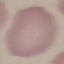
Summary:
  - Malaria status: uninfected
  - Stain: Giemsa
  - Preparation: thin blood smear
  - Image type: automatically extracted cell patch, resized to 64 × 64 pixels
  - Capture: smartphone through the microscope eyepiece